Outline each uninfected red blood cell.
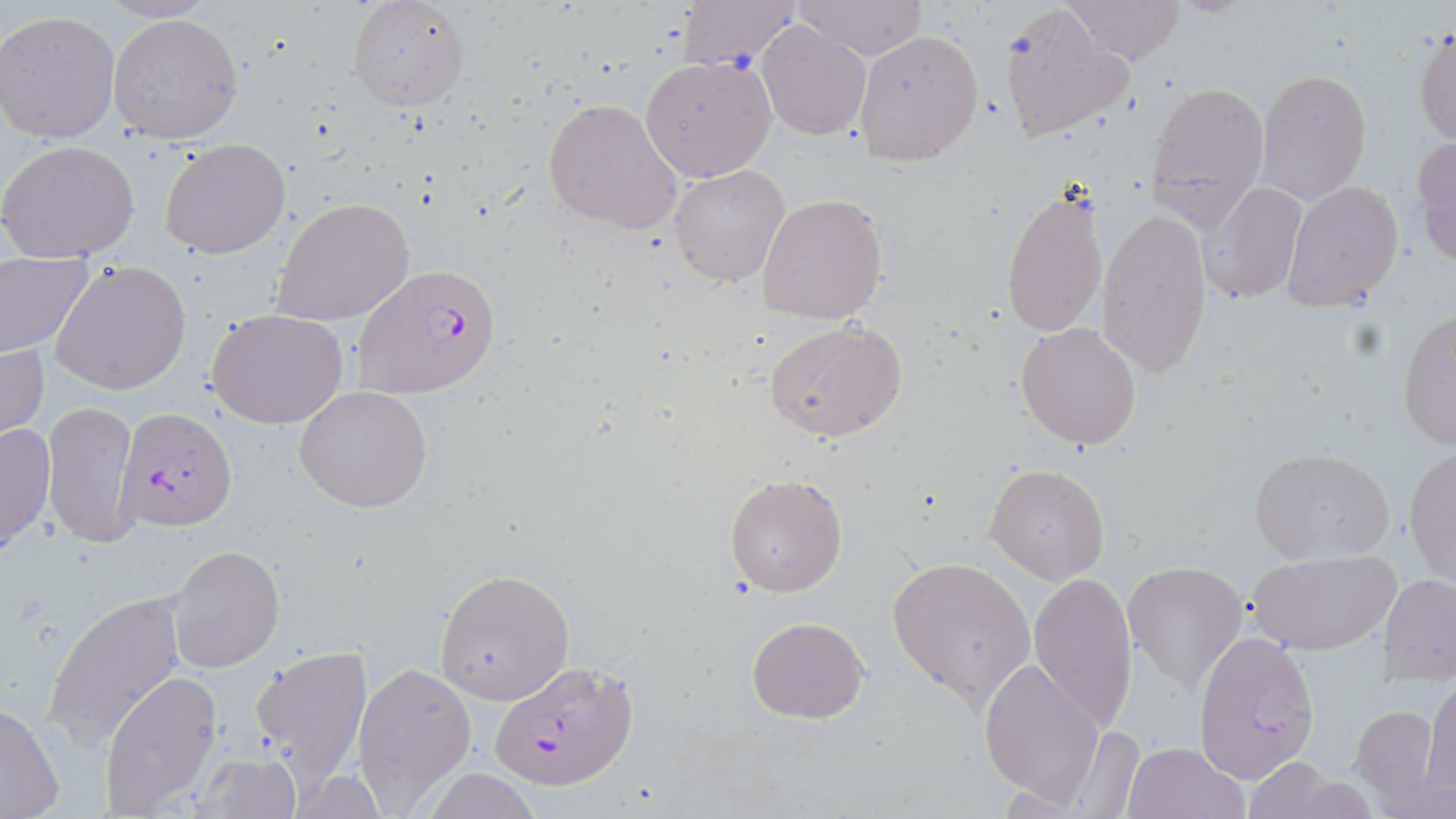

Approximate bounding boxes as named x1/y1/x2/y2 corners in pixels.
Uninfected red blood cells: (x1=346, y1=0, x2=469, y2=111), (x1=676, y1=0, x2=799, y2=68), (x1=795, y1=0, x2=929, y2=60), (x1=1059, y1=0, x2=1186, y2=65), (x1=997, y1=1, x2=1132, y2=143), (x1=0, y1=11, x2=121, y2=144), (x1=108, y1=11, x2=243, y2=146), (x1=756, y1=21, x2=871, y2=140), (x1=1413, y1=27, x2=1456, y2=150), (x1=853, y1=28, x2=983, y2=165), (x1=640, y1=55, x2=776, y2=181), (x1=1255, y1=68, x2=1373, y2=205), (x1=1144, y1=80, x2=1269, y2=226), (x1=543, y1=97, x2=683, y2=234), (x1=1413, y1=135, x2=1456, y2=268), (x1=159, y1=136, x2=292, y2=258), (x1=0, y1=139, x2=141, y2=264), (x1=668, y1=164, x2=790, y2=287), (x1=1282, y1=180, x2=1403, y2=311), (x1=1200, y1=181, x2=1307, y2=306), (x1=1000, y1=188, x2=1108, y2=339), (x1=756, y1=191, x2=889, y2=325), (x1=272, y1=198, x2=415, y2=326), (x1=1097, y1=208, x2=1212, y2=378), (x1=0, y1=252, x2=93, y2=360), (x1=50, y1=259, x2=192, y2=395), (x1=207, y1=309, x2=350, y2=429), (x1=1398, y1=309, x2=1456, y2=450), (x1=763, y1=318, x2=907, y2=443), (x1=1015, y1=321, x2=1143, y2=449), (x1=0, y1=337, x2=49, y2=448), (x1=294, y1=385, x2=434, y2=514), (x1=44, y1=399, x2=139, y2=551), (x1=0, y1=421, x2=56, y2=559), (x1=1403, y1=446, x2=1456, y2=589), (x1=1249, y1=447, x2=1395, y2=565), (x1=985, y1=464, x2=1110, y2=583), (x1=723, y1=470, x2=849, y2=597), (x1=166, y1=544, x2=285, y2=674), (x1=1248, y1=550, x2=1399, y2=656), (x1=887, y1=555, x2=1035, y2=710), (x1=1124, y1=558, x2=1248, y2=691), (x1=432, y1=568, x2=574, y2=705), (x1=1028, y1=571, x2=1139, y2=733), (x1=1379, y1=573, x2=1455, y2=684), (x1=43, y1=593, x2=187, y2=746), (x1=746, y1=615, x2=869, y2=724), (x1=1193, y1=627, x2=1320, y2=781), (x1=249, y1=645, x2=372, y2=789), (x1=979, y1=657, x2=1105, y2=806), (x1=353, y1=661, x2=476, y2=810), (x1=100, y1=670, x2=224, y2=815), (x1=1424, y1=678, x2=1456, y2=803), (x1=1, y1=699, x2=67, y2=818), (x1=1351, y1=703, x2=1446, y2=812), (x1=1066, y1=726, x2=1146, y2=817), (x1=1124, y1=741, x2=1247, y2=819), (x1=190, y1=753, x2=300, y2=816).

Plasmodium falciparum-infected red blood cell locations = approximate bounding boxes as named x1/y1/x2/y2 corners in pixels: (x1=354, y1=263, x2=501, y2=396), (x1=115, y1=405, x2=238, y2=536), (x1=491, y1=662, x2=640, y2=793)
slide-level diagnosis = Plasmodium falciparum
image size = 1456×819 pixels
stain = May-Grünwald-Giemsa
preparation = thin blood smear
modality = light microscopy
magnification = 1000x
field of view = single